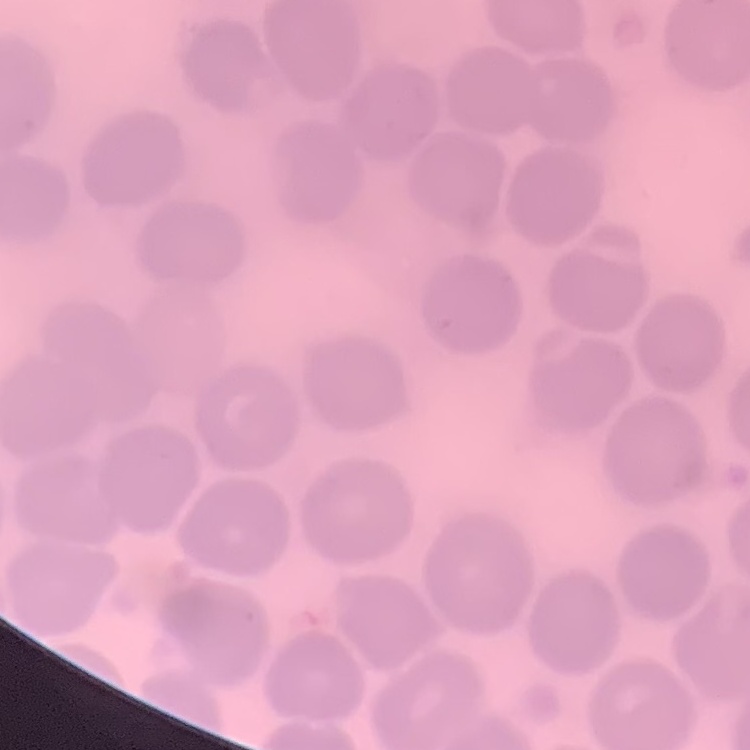
erythrocyte morphology = no rouleaux formation
preparation = thin blood film
stain = Field's or Giemsa
image type = square crop of a larger photomicrograph